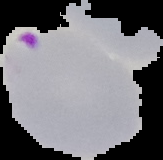

Image is 163×160 pixels. From a thin blood smear. Malaria status: parasitized. Segmented cell region on a black background.